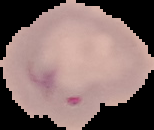
Summary:
  - Image size: 154×130 pixels
  - Result: Plasmodium parasites identified
  - Preparation: thin blood film
  - Image type: segmented cell region on a black background